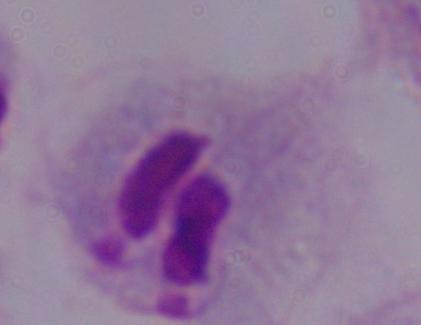

{
  "identification": "trichomonad",
  "modality": "photomicrograph",
  "magnification": "1000x"
}